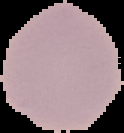

Summary:
  - Malaria status: uninfected
  - Preparation: thin blood film
  - Image size: 124×133 pixels
  - Image type: segmented cell region on a black background